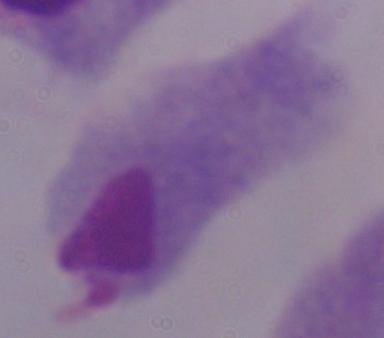

Micrograph. Captured at 1000x magnification. A trichomonad is seen.